Outline each Plasmodium vivax-infected red blood cell.
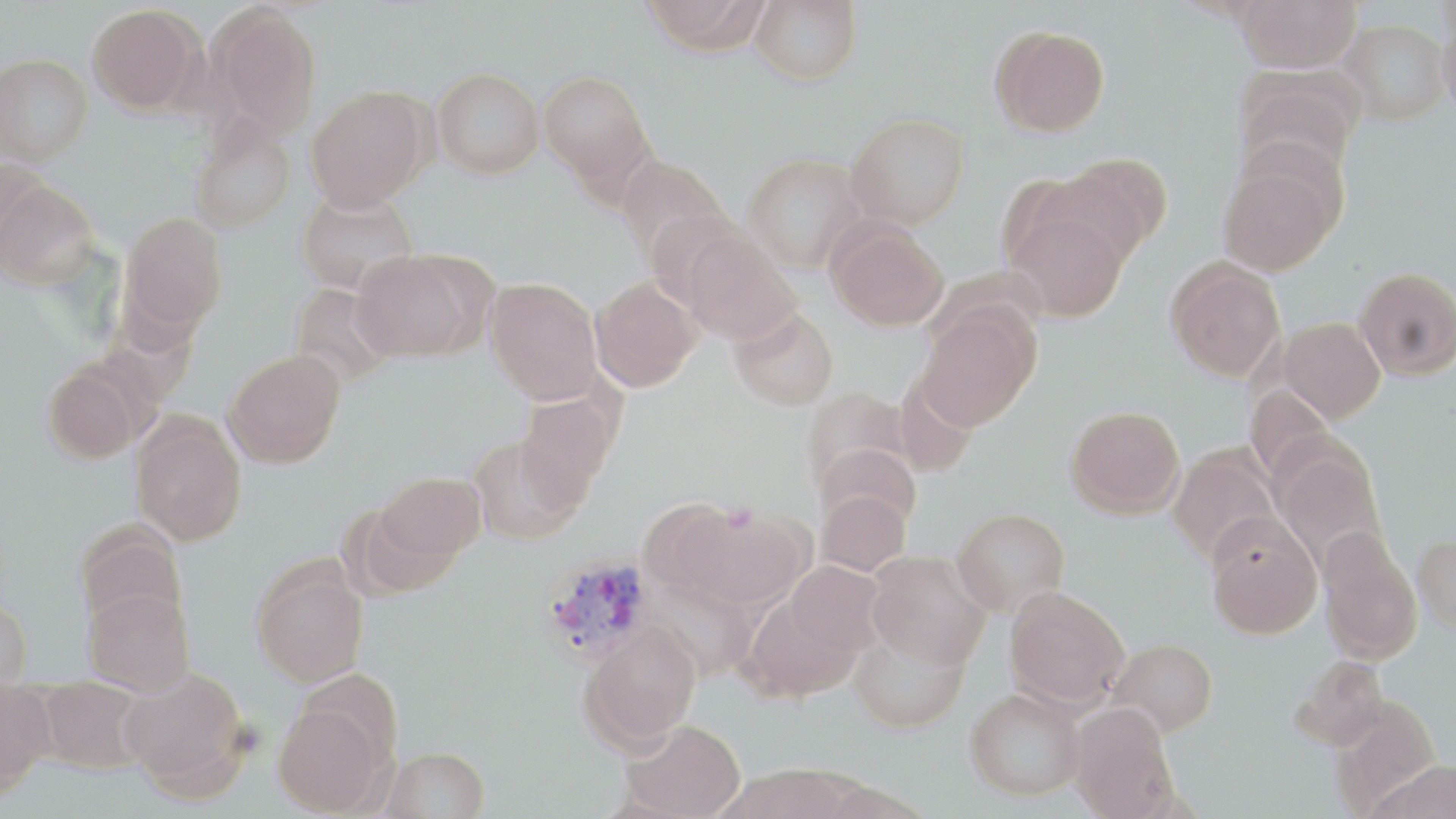
Approximate bounding boxes as (x1, y1, x2, y2) in pixels.
Plasmodium vivax-infected red blood cells: (540, 552, 656, 665).

Uninfected red blood cell locations: (639, 0, 770, 56), (749, 0, 862, 88), (1235, 0, 1360, 73), (86, 3, 202, 114), (208, 6, 323, 138), (1438, 17, 1456, 122), (1338, 19, 1449, 126), (990, 26, 1111, 139), (0, 53, 93, 164), (432, 67, 544, 178), (538, 69, 652, 185), (1235, 69, 1360, 179), (305, 86, 431, 211), (845, 113, 969, 228), (189, 115, 295, 234), (1217, 149, 1344, 277), (743, 152, 869, 272), (1056, 153, 1172, 264), (615, 155, 727, 262), (0, 156, 50, 262), (1, 181, 98, 288), (296, 189, 418, 296), (1002, 204, 1131, 323), (119, 211, 227, 338), (827, 223, 949, 333), (680, 230, 800, 345), (351, 249, 485, 362), (1165, 259, 1285, 382), (1355, 266, 1456, 381), (485, 277, 603, 405), (590, 277, 702, 392), (289, 283, 394, 387), (916, 302, 1041, 431), (730, 306, 839, 410), (1279, 317, 1385, 422), (223, 349, 345, 467), (43, 364, 141, 464), (801, 387, 914, 500), (515, 393, 617, 506), (1066, 405, 1185, 517), (131, 413, 247, 546), (469, 435, 584, 544), (813, 441, 922, 537), (1271, 441, 1387, 569), (1167, 443, 1282, 562), (376, 471, 486, 564), (815, 488, 911, 575), (637, 497, 748, 601), (952, 507, 1069, 615), (689, 508, 811, 612), (1205, 512, 1322, 639), (73, 520, 188, 633), (1317, 528, 1422, 666), (1413, 531, 1456, 636), (867, 550, 990, 670), (251, 559, 369, 687), (783, 561, 886, 662), (647, 578, 759, 680), (83, 586, 195, 696), (1004, 586, 1129, 709), (742, 591, 864, 703), (0, 594, 33, 687), (581, 620, 702, 750), (849, 628, 969, 734), (1107, 637, 1218, 737), (1292, 655, 1390, 750), (119, 667, 250, 796), (35, 678, 148, 772), (0, 680, 55, 795), (965, 688, 1085, 801), (1330, 696, 1442, 812), (272, 700, 388, 816), (1069, 703, 1180, 818), (623, 719, 745, 819), (380, 746, 490, 819), (1364, 758, 1456, 819), (720, 765, 856, 819). Slide-level diagnosis: Plasmodium vivax. 1000x magnification. Image is 1456×819 pixels. May-Grünwald-Giemsa-stained preparation. Optical microscopy. One field of a larger specimen. Thin blood film.